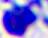

Summary:
  - Magnification: 400x
  - Modality: photomicrograph
  - Identification: leukocyte